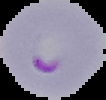

Image is 106×100 pixels. Malaria status: parasitized. Cell region segmented out of the field of view; the surrounding area is masked to black. From a thin blood film.